Locate every Plasmodium falciparum parasite and give its life-cycle stage, and locate every leukocyte and any debris.
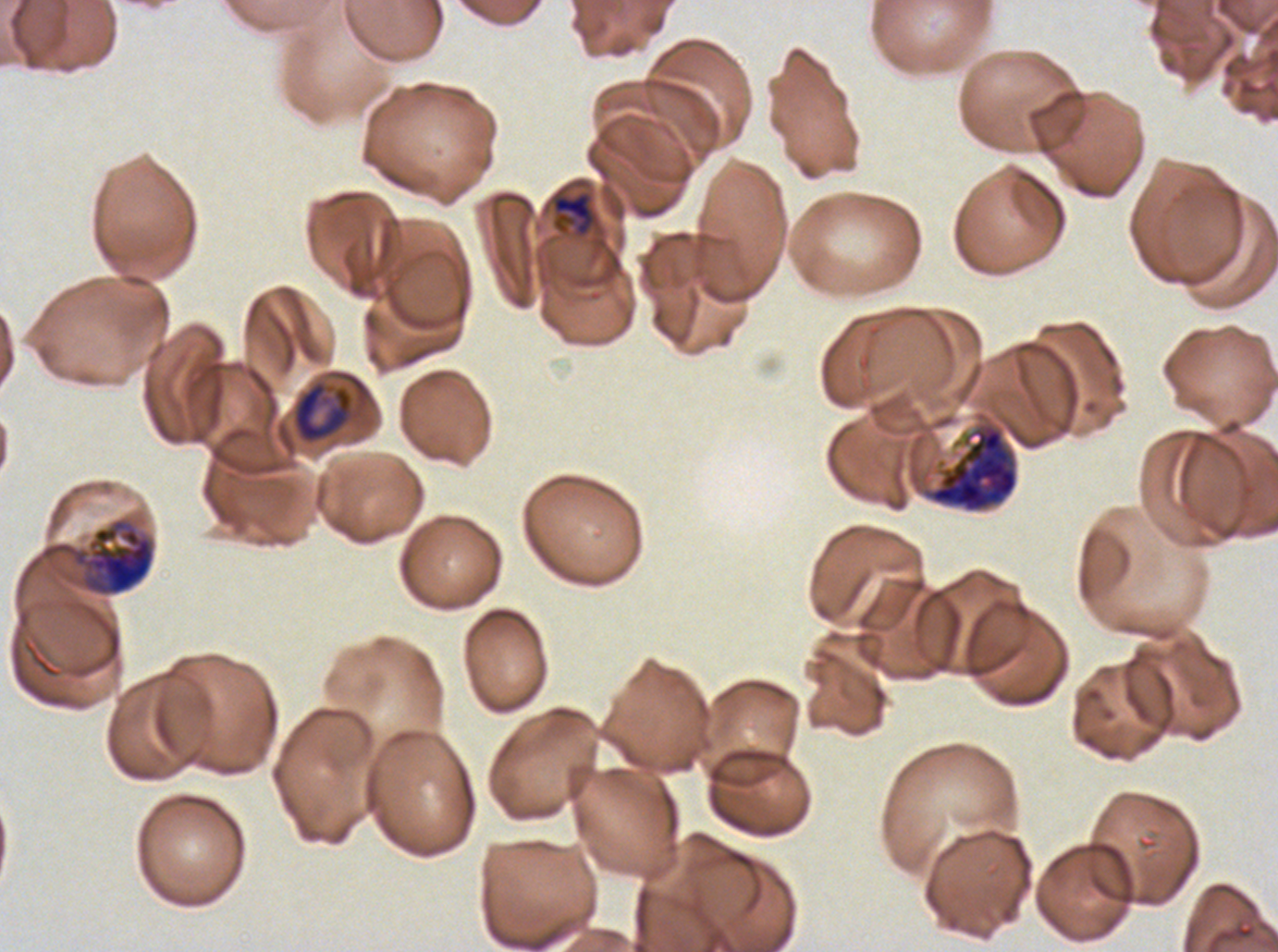

Approximate bounding boxes as {x1, y1, x2, y2} in pixels.
Late-ring/early-trophozoite forms: {551, 190, 596, 238}.
Late trophozoites: {291, 379, 354, 445}.
Early schizonts: {920, 421, 1019, 514}, {41, 518, 155, 596}.
No rings, mid trophozoites, late schizonts, segmenters, gametocytes, leukocytes, or debris observed.

Summary:
  - Stain: Giemsa
  - Specimen: ex-vivo Plasmodium falciparum culture from a patient in The Gambia, grown for 24 to 48 hours
  - Preparation: thin blood smear
  - Field of view: sub-image separated from a larger composite
  - Image size: 1278×952 pixels
  - Life-cycle stages observed: late-ring/early-trophozoite, late trophozoite, early schizont